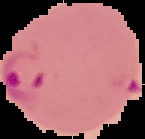 From a thin blood film. Segmented cell region on a black background. Image is 145×139 pixels. Malaria status: parasitized.